Classify this cell by malaria status.
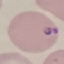

It is parasitized.

Summary:
  - Capture: smartphone camera at the microscope eyepiece
  - Image type: cell patch, automatically extracted from a larger field of view and resized to 64 × 64 pixels
  - Preparation: thin blood film
  - Stain: Giemsa